Point out every Plasmodium parasite and every leukocyte.
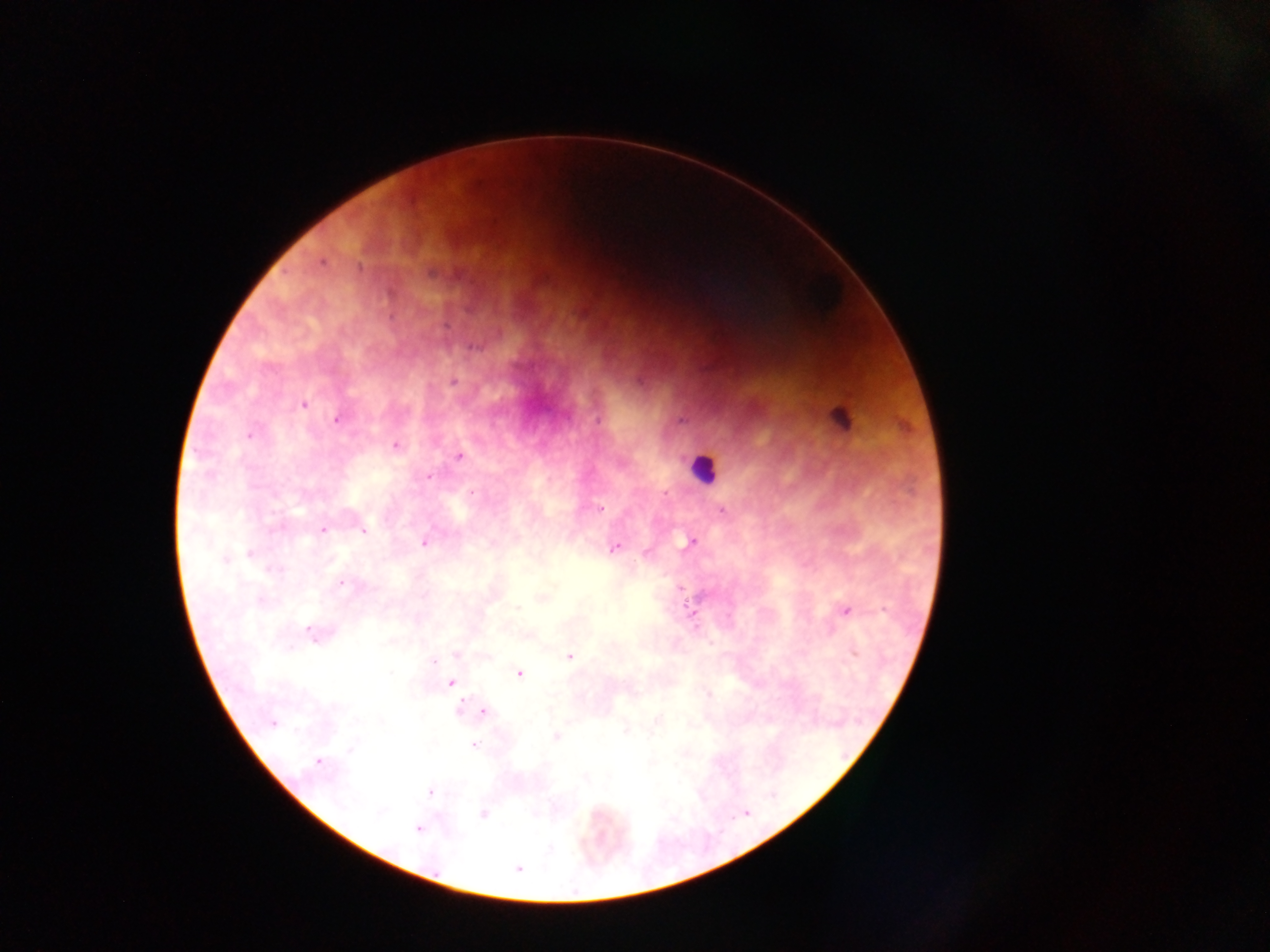

Approximate centers as (x, y) in pixels.
Plasmodium parasites: (321, 262), (433, 272), (474, 348), (454, 382), (303, 405), (337, 419), (598, 421), (682, 421), (248, 435), (396, 446), (459, 456), (428, 477), (666, 492), (472, 493), (601, 508), (722, 510), (323, 530), (363, 531), (692, 541), (424, 542), (615, 548), (251, 553), (225, 560), (273, 570), (341, 583), (680, 588), (259, 601), (517, 608), (846, 611), (311, 631), (855, 653), (457, 655), (569, 657), (433, 662), (519, 674), (450, 683), (460, 709), (483, 712), (273, 723), (556, 737), (473, 745), (317, 762), (430, 792), (380, 812), (483, 814), (418, 829), (518, 869).
Leukocytes: (824, 294), (703, 468).
One object is labeled both Plasmodium parasite and leukocyte by the source: (841, 418).

Summary:
  - Image size: 1270×952 pixels
  - Field of view: single
  - Country: Ghana
  - Capture: mobile-phone photograph through a microscope
  - Preparation: thick blood smear